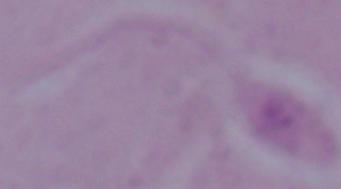
Summary:
  - Magnification: 1000x
  - Modality: photomicrograph
  - Identification: Leishmania